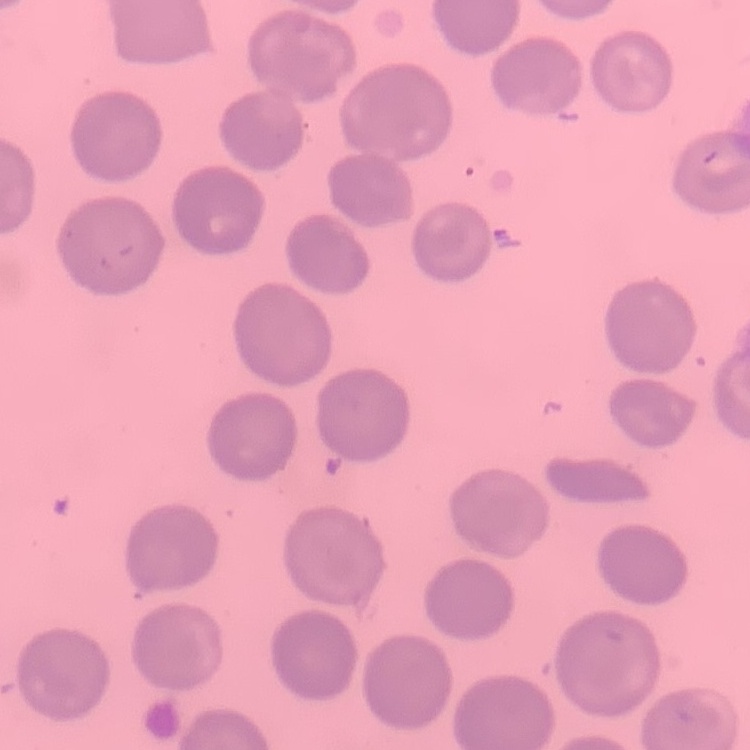

{
  "erythrocyte_morphology": "no rouleaux formation",
  "preparation": "thin peripheral smear",
  "image_type": "square crop of a larger photomicrograph",
  "stain": "Field's or Giemsa"
}